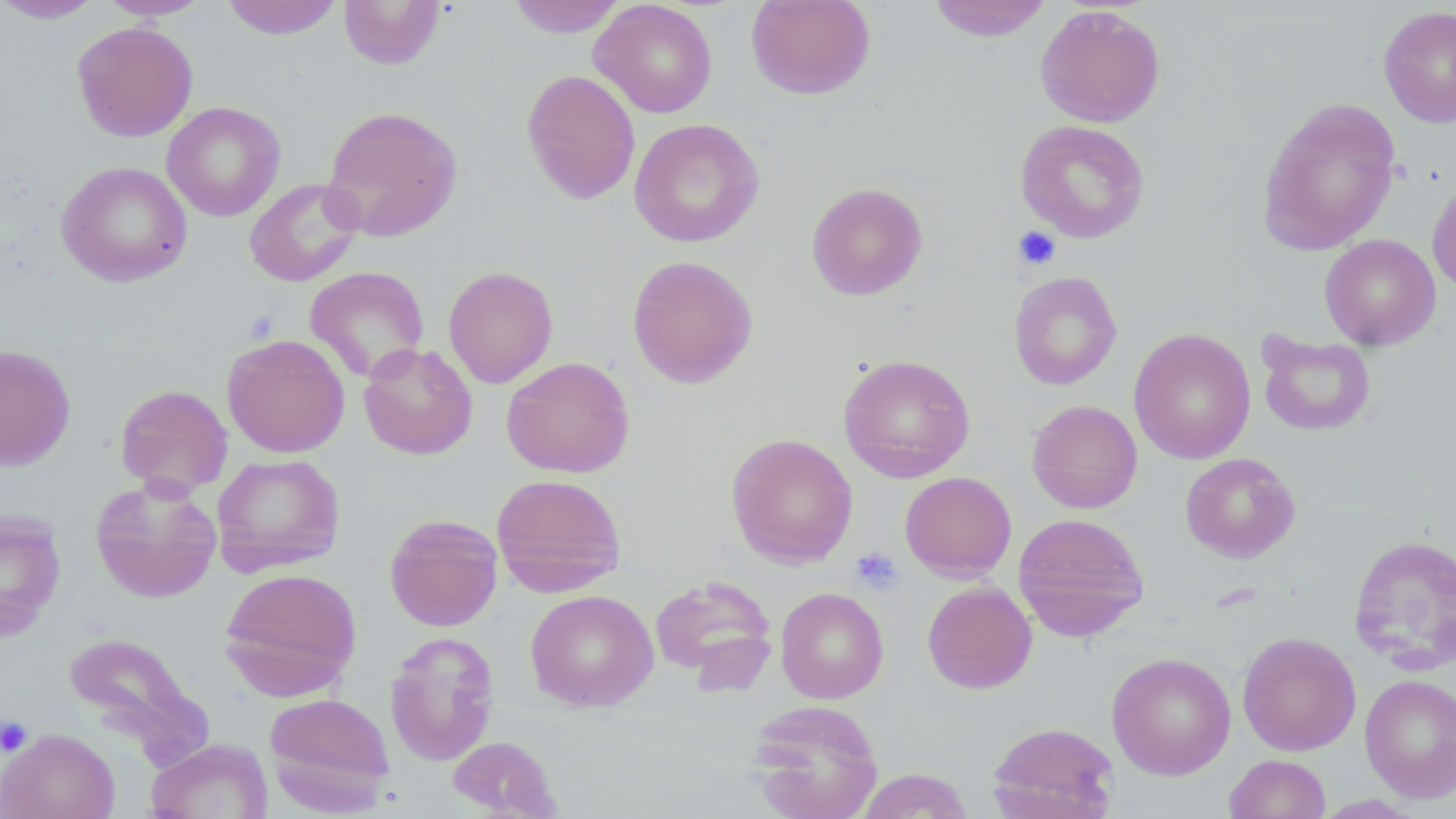
Approximate bounding boxes as named x1/y1/x2/y2 corners in pixels. Platelet locations: (x1=1012, y1=226, x2=1061, y2=270), (x1=849, y1=548, x2=903, y2=595), (x1=0, y1=715, x2=33, y2=758). Uninfected red blood cell locations: (x1=0, y1=0, x2=107, y2=24), (x1=97, y1=0, x2=211, y2=20), (x1=220, y1=0, x2=345, y2=40), (x1=339, y1=0, x2=445, y2=70), (x1=507, y1=0, x2=627, y2=38), (x1=590, y1=0, x2=718, y2=118), (x1=746, y1=0, x2=876, y2=100), (x1=926, y1=0, x2=1053, y2=42), (x1=1035, y1=4, x2=1166, y2=127), (x1=1378, y1=5, x2=1456, y2=128), (x1=72, y1=21, x2=198, y2=142), (x1=521, y1=69, x2=640, y2=205), (x1=1256, y1=96, x2=1402, y2=256), (x1=162, y1=101, x2=286, y2=222), (x1=321, y1=105, x2=463, y2=242), (x1=629, y1=118, x2=765, y2=248), (x1=1014, y1=120, x2=1150, y2=243), (x1=56, y1=161, x2=193, y2=287), (x1=1427, y1=175, x2=1456, y2=294), (x1=244, y1=177, x2=364, y2=287), (x1=806, y1=181, x2=928, y2=301), (x1=1319, y1=233, x2=1441, y2=350), (x1=626, y1=254, x2=758, y2=389), (x1=304, y1=266, x2=429, y2=382), (x1=443, y1=266, x2=558, y2=389), (x1=1008, y1=270, x2=1123, y2=390), (x1=1129, y1=328, x2=1256, y2=464), (x1=1256, y1=330, x2=1377, y2=437), (x1=222, y1=334, x2=350, y2=457), (x1=358, y1=342, x2=478, y2=460), (x1=0, y1=344, x2=76, y2=470), (x1=837, y1=353, x2=976, y2=483), (x1=501, y1=356, x2=635, y2=478), (x1=115, y1=383, x2=233, y2=497), (x1=1026, y1=399, x2=1143, y2=514), (x1=725, y1=432, x2=858, y2=569), (x1=1180, y1=452, x2=1301, y2=563), (x1=211, y1=453, x2=346, y2=577), (x1=899, y1=471, x2=1016, y2=581), (x1=491, y1=473, x2=627, y2=596), (x1=89, y1=477, x2=222, y2=604), (x1=0, y1=509, x2=66, y2=642), (x1=1013, y1=512, x2=1149, y2=642), (x1=384, y1=514, x2=503, y2=632), (x1=1347, y1=533, x2=1456, y2=675), (x1=218, y1=567, x2=362, y2=701), (x1=649, y1=574, x2=778, y2=687), (x1=922, y1=581, x2=1037, y2=694), (x1=775, y1=587, x2=889, y2=704), (x1=525, y1=589, x2=659, y2=712), (x1=63, y1=631, x2=208, y2=759), (x1=384, y1=631, x2=500, y2=767), (x1=1237, y1=631, x2=1361, y2=755), (x1=1107, y1=652, x2=1237, y2=779), (x1=1360, y1=674, x2=1456, y2=802), (x1=264, y1=691, x2=395, y2=814), (x1=747, y1=699, x2=884, y2=819), (x1=987, y1=721, x2=1120, y2=819), (x1=1, y1=728, x2=120, y2=819), (x1=446, y1=736, x2=561, y2=818), (x1=146, y1=738, x2=273, y2=819), (x1=1223, y1=753, x2=1331, y2=818), (x1=855, y1=768, x2=974, y2=818). Slide-level diagnosis: negative for blood parasites. May-Grünwald-Giemsa stain. One field of a larger specimen. 1000x magnification. Thin blood smear. Image is 1456×819 pixels. Light microscopy.